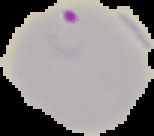

Image is 154×136 pixels. The area outside the segmented cell region is set to black. From a thin blood film. Result: malaria parasites detected.